Point out every Plasmodium parasite and every leukocyte.
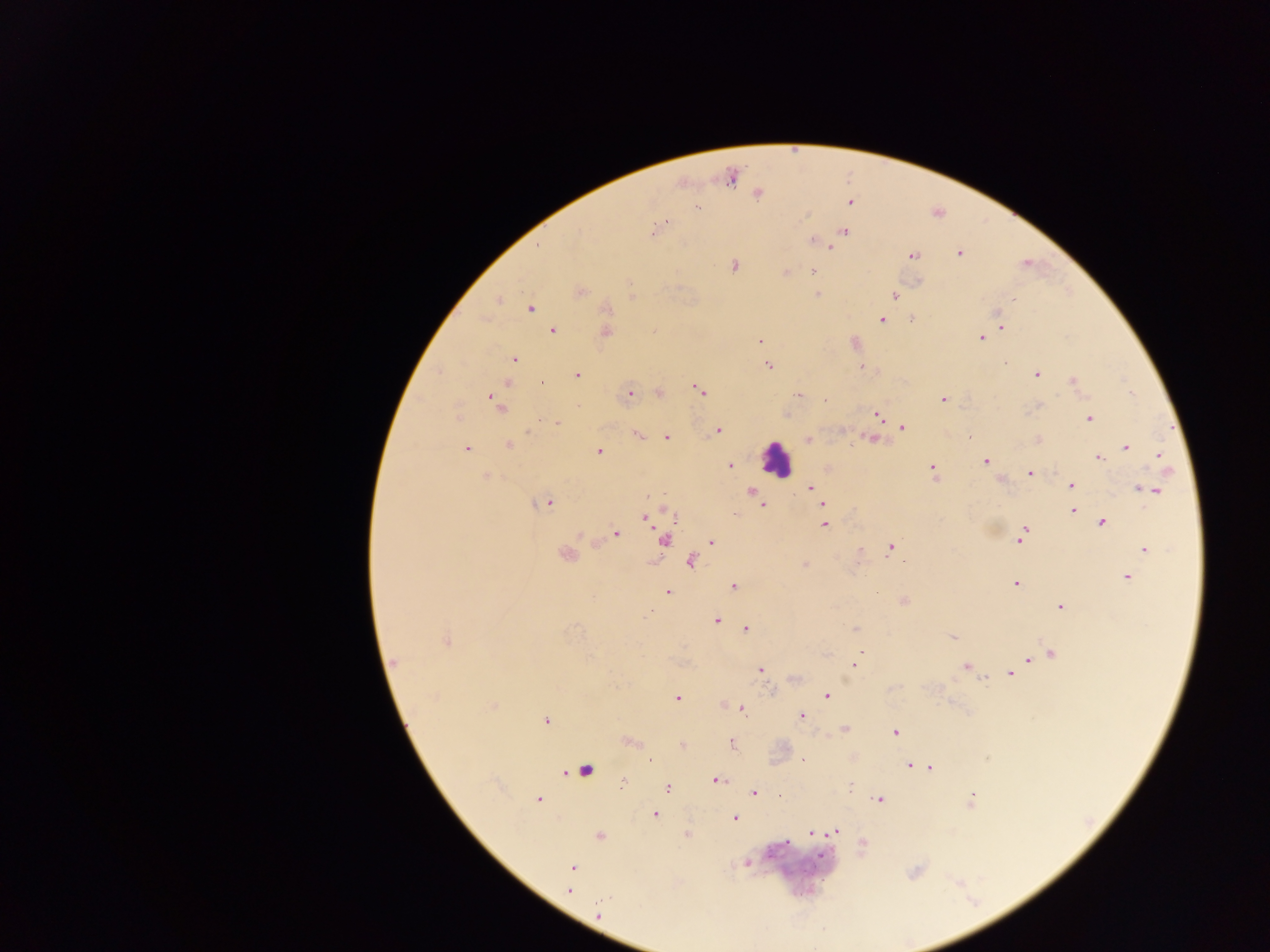
Approximate centers as {x, y} in pixels.
Plasmodium parasites: {758, 194}, {851, 202}, {697, 207}, {660, 227}, {655, 230}, {844, 231}, {813, 240}, {819, 243}, {831, 248}, {960, 254}, {912, 255}, {733, 265}, {814, 271}, {785, 272}, {580, 291}, {818, 295}, {894, 295}, {1013, 299}, {498, 300}, {530, 309}, {606, 309}, {881, 320}, {912, 320}, {1002, 326}, {553, 331}, {606, 332}, {980, 338}, {760, 341}, {514, 358}, {768, 365}, {861, 367}, {577, 375}, {1037, 375}, {1072, 380}, {542, 382}, {699, 389}, {659, 393}, {629, 395}, {798, 395}, {826, 399}, {944, 399}, {495, 400}, {876, 414}, {1089, 419}, {557, 423}, {903, 427}, {717, 430}, {639, 435}, {666, 437}, {809, 439}, {868, 439}, {509, 445}, {1126, 446}, {467, 449}, {598, 452}, {1161, 455}, {1098, 457}, {986, 462}, {730, 466}, {932, 468}, {1030, 473}, {486, 476}, {1001, 480}, {1072, 485}, {811, 487}, {1151, 490}, {815, 492}, {752, 493}, {545, 503}, {823, 503}, {762, 505}, {1072, 510}, {1076, 513}, {645, 517}, {1102, 522}, {825, 524}, {1024, 529}, {616, 533}, {1021, 538}, {711, 541}, {860, 549}, {890, 549}, {1145, 549}, {566, 555}, {690, 561}, {804, 565}, {1127, 577}, {1016, 584}, {734, 586}, {668, 592}, {903, 601}, {1061, 607}, {717, 620}, {746, 628}, {856, 629}, {952, 637}, {446, 641}, {860, 652}, {1051, 654}, {1042, 656}, {1028, 660}, {395, 662}, {854, 665}, {966, 667}, {760, 669}, {1010, 674}, {827, 696}, {678, 699}, {493, 706}, {742, 709}, {801, 716}, {546, 721}, {845, 729}, {895, 733}, {631, 741}, {731, 743}, {648, 760}, {803, 760}, {909, 765}, {931, 768}, {716, 780}, {622, 782}, {667, 787}, {850, 788}, {754, 793}, {972, 797}, {538, 799}, {878, 800}, {655, 814}, {735, 818}, {836, 832}, {811, 833}, {599, 836}, {862, 843}, {572, 867}, {570, 889}, {598, 911}.
Leukocytes: {776, 458}, {661, 537}, {584, 770}.

Thick blood film. Sample from Ghana. Mobile-phone photograph taken through the microscope. One field of view. Image is 1270×952 pixels.